Assess this cell for malaria.
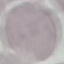
Uninfected.

Summary:
  - Capture: smartphone through the microscope eyepiece
  - Preparation: thin smear
  - Image type: cell patch, automatically extracted from a larger field of view and resized to 64 × 64 pixels
  - Stain: Giemsa